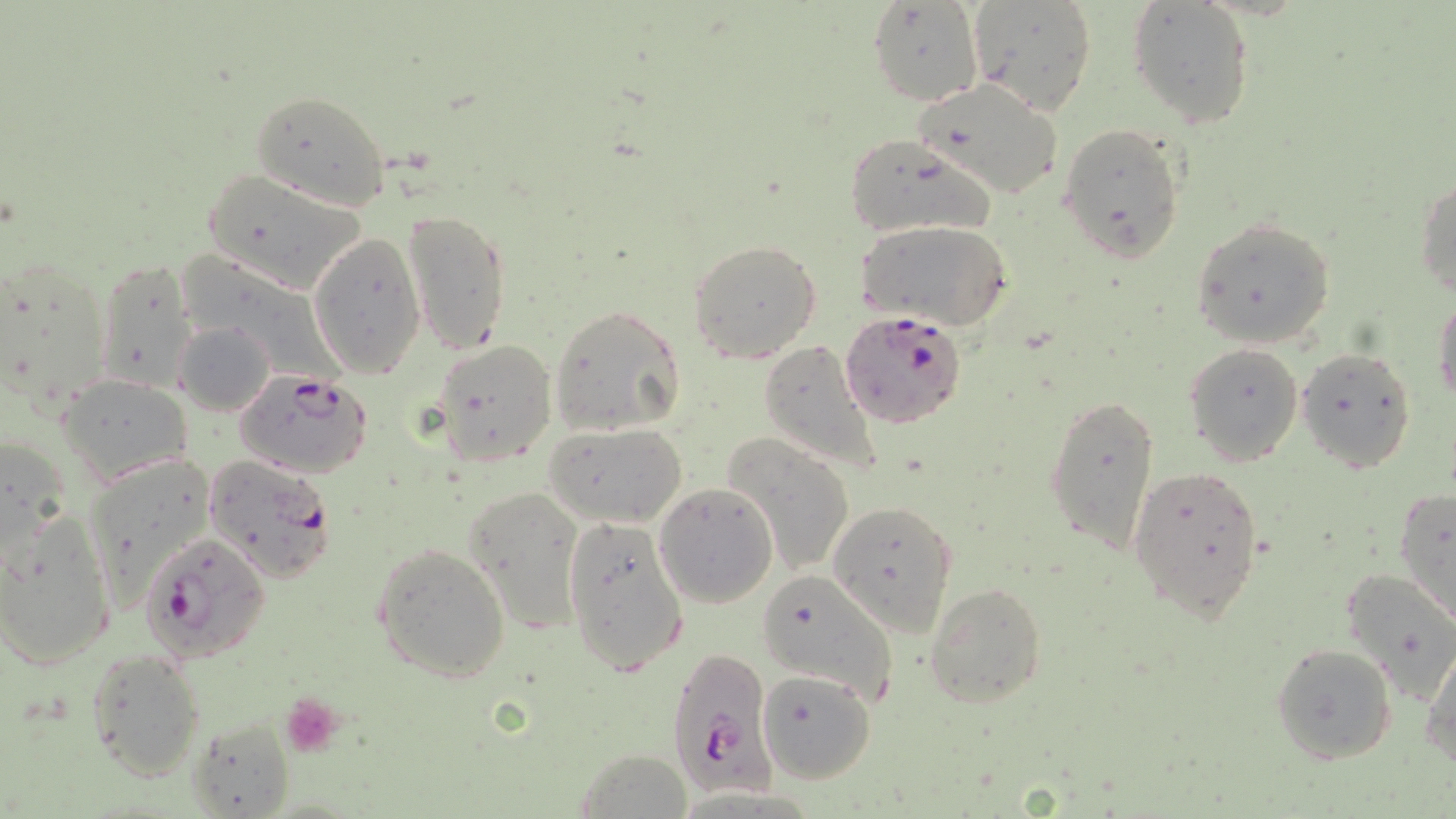
Approximate bounding boxes as (x1,y1)-(x2,y2) corner pairs in pixels. Platelet locations: (282,692)-(345,756). Uninfected red blood cell locations: (868,1)-(985,106), (966,1)-(1097,117), (1128,1)-(1255,130), (915,76)-(1066,201), (249,91)-(390,210), (1057,123)-(1186,264), (842,137)-(998,241), (203,167)-(368,294), (1415,177)-(1456,299), (402,207)-(510,355), (1190,216)-(1336,349), (859,220)-(1013,332), (307,232)-(427,380), (688,239)-(822,363), (5,256)-(116,410), (95,256)-(199,393), (1432,294)-(1456,412), (549,305)-(685,436), (176,320)-(276,415), (432,339)-(556,466), (758,341)-(883,478), (1185,344)-(1303,466), (1295,347)-(1416,472), (59,374)-(191,483), (1043,388)-(1161,558), (544,421)-(687,529), (723,434)-(855,577), (0,440)-(72,558), (80,455)-(215,602), (1127,464)-(1266,624), (654,482)-(780,607), (465,485)-(585,634), (1393,487)-(1456,626), (830,500)-(956,636), (1,511)-(116,671), (561,515)-(690,679), (371,542)-(511,683), (1341,566)-(1456,701), (757,569)-(901,706), (925,581)-(1048,709), (1272,642)-(1398,764), (1422,643)-(1456,769), (83,647)-(209,783), (758,668)-(876,784), (186,714)-(298,818), (573,748)-(695,817). Plasmodium falciparum-infected red blood cell locations: (839,309)-(968,429), (235,370)-(375,480), (203,456)-(339,583), (140,530)-(269,662), (665,646)-(776,799). Slide-level diagnosis: Plasmodium falciparum. Image is 1456×819 pixels. Optical microscopy. One field of a larger specimen. May-Grünwald-Giemsa stain. 1000x magnification. Thin blood smear.